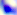

Captured at 400x magnification. Toxoplasma gondii is shown. Micrograph.